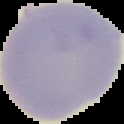 The area outside the segmented cell region is set to black. Result: no Plasmodium parasites detected. From a thin blood smear. Image is 124×124 pixels.